Locate and identify every blood parasite.
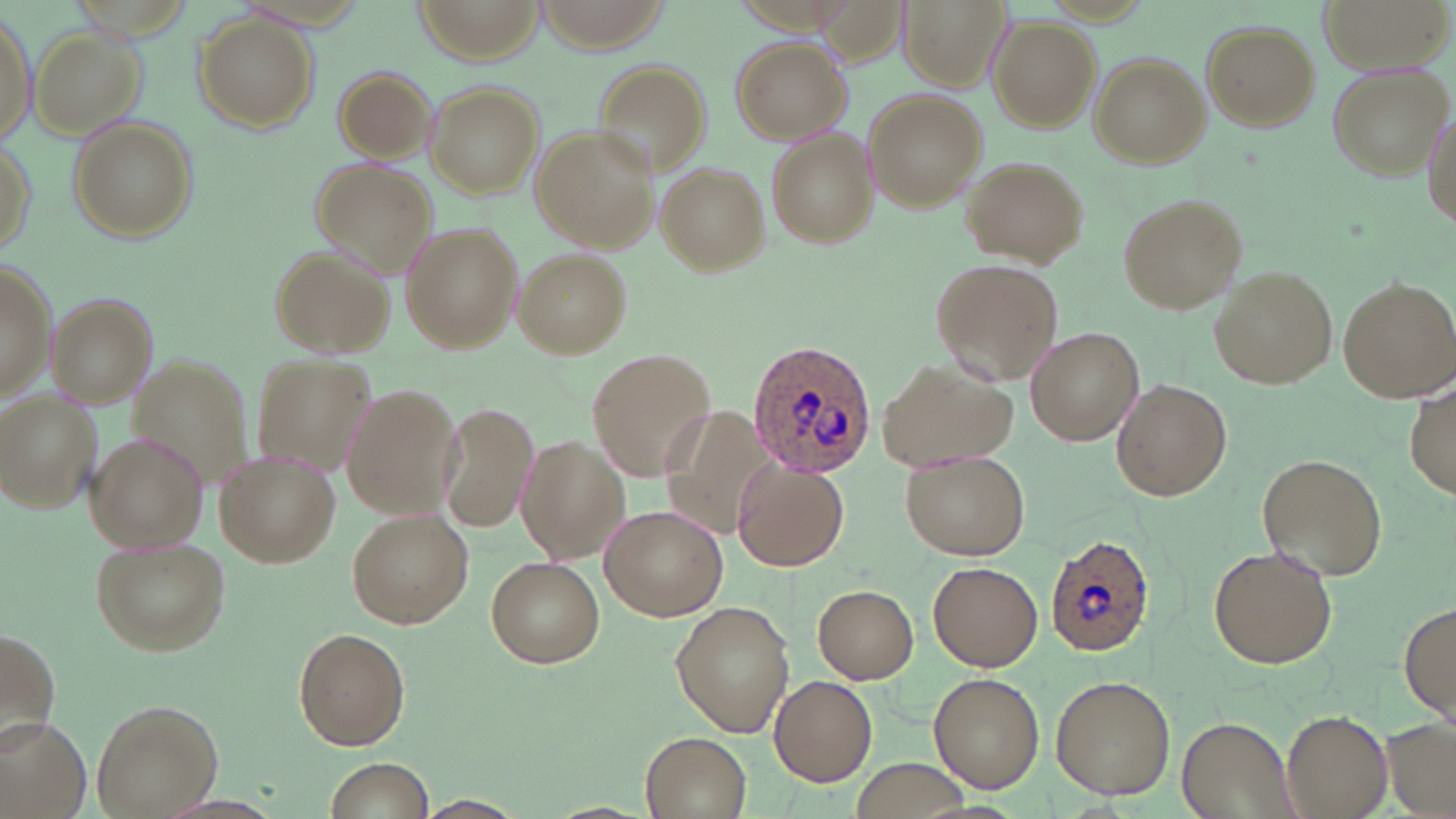
Approximate bounding boxes as named x1/y1/x2/y2 corners in pixels.
Plasmodium ovale-infected red blood cells: (x1=746, y1=337, x2=880, y2=475), (x1=1045, y1=531, x2=1154, y2=655).
No Plasmodium falciparum, Plasmodium malariae, Plasmodium vivax, Babesia divergens, or Trypanosoma brucei observed.

Summary:
  - Uninfected red blood cell locations: (x1=412, y1=0, x2=545, y2=64), (x1=899, y1=0, x2=1012, y2=93), (x1=1321, y1=0, x2=1449, y2=70), (x1=1, y1=11, x2=36, y2=151), (x1=191, y1=12, x2=319, y2=132), (x1=987, y1=16, x2=1099, y2=131), (x1=1199, y1=19, x2=1321, y2=131), (x1=35, y1=28, x2=144, y2=137), (x1=729, y1=36, x2=852, y2=143), (x1=1088, y1=52, x2=1210, y2=168), (x1=591, y1=58, x2=712, y2=175), (x1=1326, y1=62, x2=1450, y2=179), (x1=331, y1=65, x2=440, y2=163), (x1=426, y1=81, x2=545, y2=199), (x1=863, y1=87, x2=986, y2=212), (x1=1423, y1=105, x2=1456, y2=232), (x1=69, y1=117, x2=196, y2=241), (x1=530, y1=124, x2=659, y2=253), (x1=767, y1=128, x2=879, y2=250), (x1=0, y1=135, x2=36, y2=261), (x1=312, y1=157, x2=436, y2=277), (x1=964, y1=157, x2=1085, y2=266), (x1=657, y1=162, x2=770, y2=275), (x1=1117, y1=192, x2=1246, y2=315), (x1=400, y1=222, x2=523, y2=354), (x1=269, y1=245, x2=392, y2=357), (x1=515, y1=248, x2=631, y2=357), (x1=931, y1=258, x2=1062, y2=387), (x1=0, y1=263, x2=55, y2=402), (x1=1210, y1=265, x2=1337, y2=389), (x1=1338, y1=276, x2=1456, y2=402), (x1=46, y1=294, x2=158, y2=407), (x1=1027, y1=327, x2=1143, y2=444), (x1=585, y1=349, x2=717, y2=482), (x1=123, y1=350, x2=266, y2=493), (x1=255, y1=356, x2=380, y2=475), (x1=879, y1=359, x2=1021, y2=471), (x1=1407, y1=377, x2=1455, y2=502), (x1=1111, y1=380, x2=1232, y2=501), (x1=342, y1=384, x2=468, y2=519), (x1=2, y1=391, x2=101, y2=514), (x1=438, y1=402, x2=539, y2=536), (x1=661, y1=407, x2=788, y2=541), (x1=86, y1=432, x2=209, y2=552), (x1=515, y1=436, x2=627, y2=566), (x1=901, y1=449, x2=1030, y2=561), (x1=216, y1=450, x2=343, y2=567), (x1=1256, y1=453, x2=1388, y2=581), (x1=733, y1=456, x2=851, y2=572), (x1=599, y1=506, x2=729, y2=621), (x1=347, y1=509, x2=473, y2=628), (x1=90, y1=535, x2=229, y2=655), (x1=1208, y1=545, x2=1339, y2=668), (x1=488, y1=557, x2=604, y2=668), (x1=930, y1=562, x2=1042, y2=672), (x1=814, y1=584, x2=918, y2=683), (x1=1398, y1=600, x2=1456, y2=725), (x1=670, y1=601, x2=795, y2=736), (x1=0, y1=626, x2=59, y2=747), (x1=293, y1=627, x2=411, y2=750), (x1=928, y1=672, x2=1045, y2=791), (x1=769, y1=674, x2=878, y2=786), (x1=1050, y1=676, x2=1175, y2=798), (x1=91, y1=696, x2=222, y2=817), (x1=1281, y1=707, x2=1393, y2=818), (x1=1379, y1=715, x2=1456, y2=819), (x1=1176, y1=716, x2=1299, y2=819), (x1=1, y1=717, x2=93, y2=818), (x1=640, y1=732, x2=751, y2=819), (x1=853, y1=757, x2=972, y2=819), (x1=326, y1=758, x2=437, y2=818), (x1=413, y1=795, x2=527, y2=818)
  - Slide-level diagnosis: Plasmodium ovale
  - Stain: May-Grünwald-Giemsa
  - Image size: 1456×819 pixels
  - Modality: optical microscopy
  - Magnification: 1000x
  - Field of view: one of a larger specimen
  - Preparation: thin blood smear